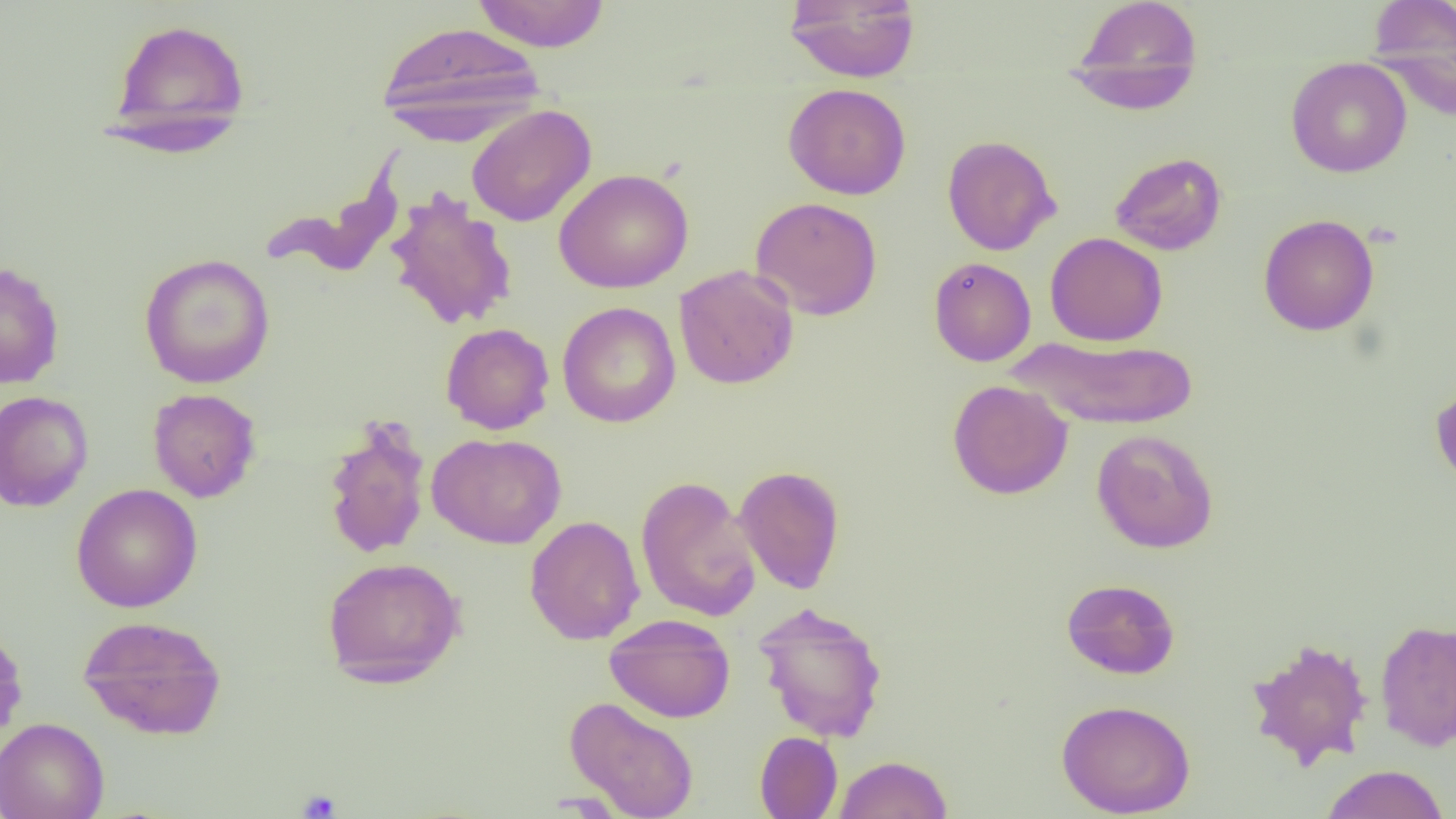
slide_level_diagnosis: no evidence of blood parasites
preparation: thin blood smear
image_size: 1456×819 pixels
field_of_view: single
uninfected_red_blood_cell_locations: 'approximate bounding boxes as (x1, y1, x2, y2) in pixels: (470, 0, 611, 52), (785, 0, 920, 83), (1068, 0, 1203, 114), (1367, 0, 1455, 104), (107, 17, 250, 151), (376, 20, 546, 141), (1286, 57, 1412, 178), (783, 83, 912, 199), (466, 105, 596, 227), (941, 135, 1061, 255), (258, 148, 406, 279), (1109, 152, 1227, 255), (554, 168, 693, 293), (384, 188, 519, 331), (750, 196, 883, 321), (1258, 214, 1379, 335), (1045, 232, 1168, 347), (138, 253, 276, 389), (929, 257, 1036, 366), (0, 261, 65, 389), (673, 265, 799, 389), (557, 301, 681, 428), (441, 322, 554, 434), (1006, 335, 1199, 430), (947, 379, 1073, 499), (1431, 381, 1456, 489), (147, 388, 262, 503), (0, 390, 94, 512), (321, 417, 432, 560), (1091, 429, 1219, 553), (426, 432, 566, 549), (734, 465, 846, 594), (635, 476, 761, 623), (71, 483, 203, 612), (524, 515, 645, 645), (321, 556, 466, 688), (1061, 578, 1180, 679), (752, 602, 888, 742), (77, 614, 227, 740), (605, 614, 736, 723), (1375, 619, 1456, 752), (0, 624, 28, 748), (1246, 637, 1374, 769), (564, 696, 700, 819), (1056, 698, 1195, 818), (0, 716, 109, 819), (754, 731, 843, 818), (833, 754, 953, 818), (1320, 764, 1449, 819)'
platelet_locations: 'approximate bounding boxes as (x1, y1, x2, y2) in pixels: (298, 787, 342, 817)'
modality: light microscopy
magnification: 1000x